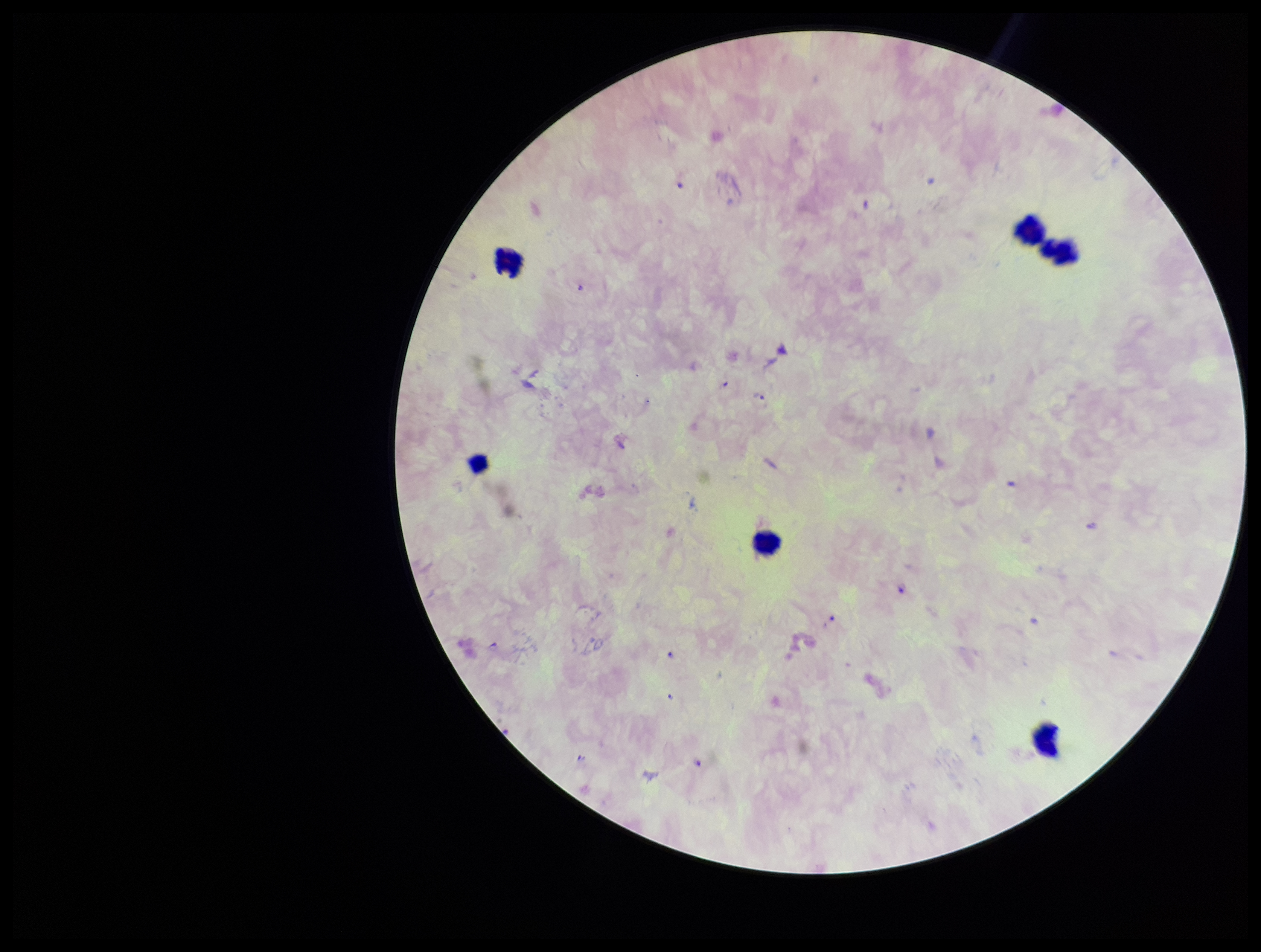

{
  "capture": "smartphone photograph through the microscope eyepiece",
  "stain": "Giemsa",
  "patient_malaria_status": "infected",
  "species_reported_for_this_patient": "Plasmodium falciparum",
  "parasite_count": 8,
  "plasmodium_parasites": "seen",
  "field_of_view": "one from this slide",
  "preparation": "thick blood smear",
  "leukocyte_count": 6,
  "image_size": "1261×952 pixels"
}